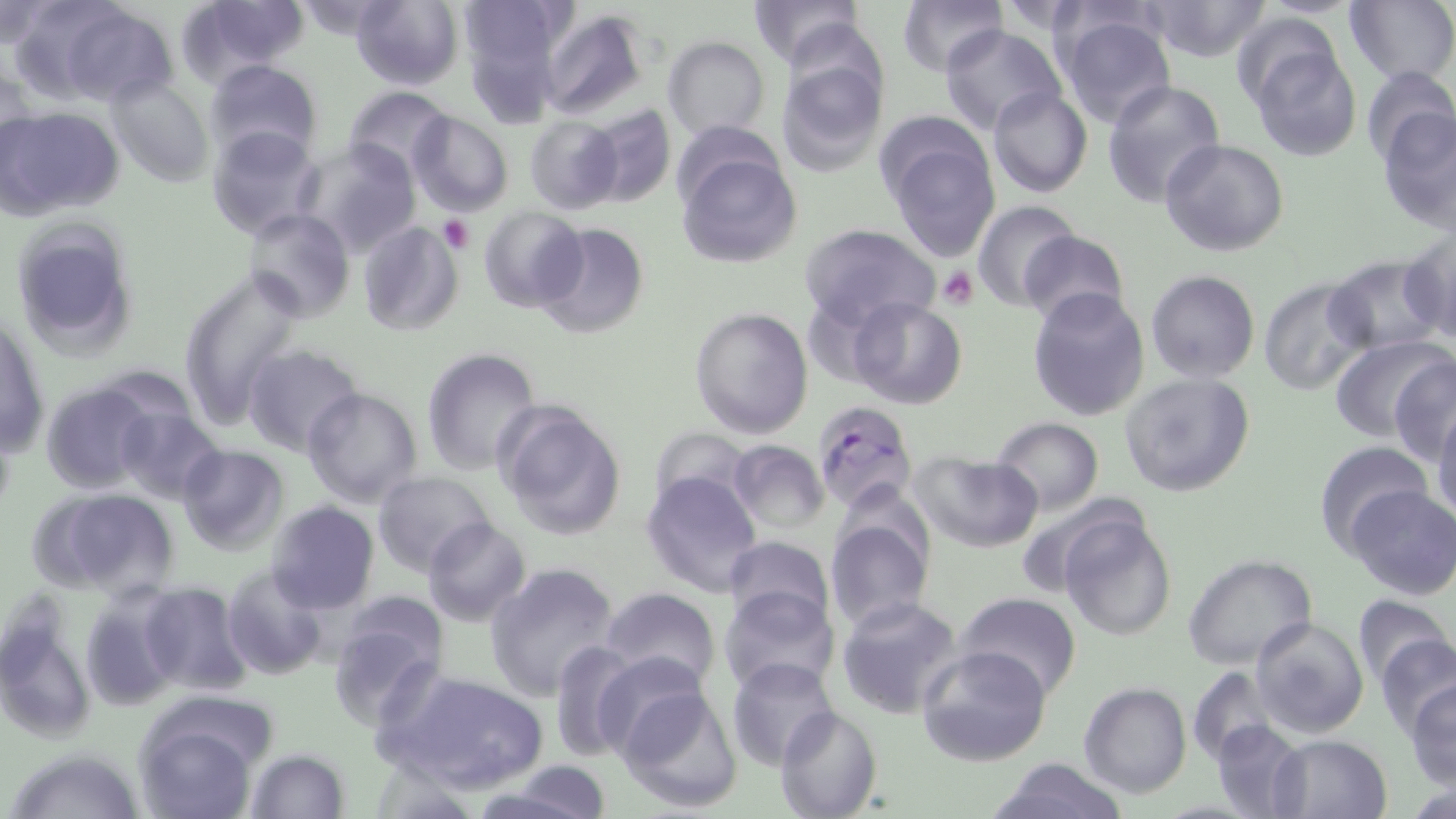
slide_level_diagnosis: Plasmodium falciparum
image_size: 1456×819 pixels
plasmodium_falciparum_infected_red_blood_cell_locations: 'approximate bounding boxes as [x1, y1, x2, y2] in pixels: [812, 401, 918, 514]'
platelet_locations: 'approximate bounding boxes as [x1, y1, x2, y2] in pixels: [439, 216, 474, 254], [938, 266, 979, 309]'
stain: May-Grünwald-Giemsa
magnification: 1000x
uninfected_red_blood_cell_locations: 'approximate bounding boxes as [x1, y1, x2, y2] in pixels: [174, 0, 307, 86], [353, 0, 463, 90], [747, 0, 862, 69], [896, 0, 1007, 77], [1144, 0, 1275, 62], [1, 2, 56, 49], [457, 2, 577, 66], [985, 2, 1103, 34], [1345, 2, 1456, 87], [55, 4, 176, 107], [539, 9, 651, 122], [1228, 11, 1344, 109], [1058, 12, 1178, 128], [938, 24, 1065, 132], [663, 36, 769, 141], [1244, 41, 1362, 162], [776, 58, 886, 178], [204, 59, 321, 164], [0, 63, 35, 173], [1359, 66, 1455, 166], [108, 76, 214, 188], [1101, 79, 1225, 208], [987, 85, 1093, 198], [344, 87, 451, 179], [580, 105, 677, 209], [1376, 105, 1456, 233], [1, 107, 123, 216], [408, 112, 513, 216], [524, 117, 623, 214], [512, 121, 611, 287], [207, 124, 321, 238], [882, 128, 1001, 261], [1160, 138, 1290, 257], [298, 140, 421, 259], [675, 144, 801, 270], [973, 200, 1081, 311], [479, 205, 587, 313], [243, 208, 353, 324], [8, 217, 143, 358], [357, 221, 464, 336], [534, 222, 649, 338], [800, 222, 940, 331], [1401, 228, 1456, 344], [1017, 229, 1129, 327], [1325, 257, 1444, 357], [176, 268, 309, 430], [1147, 271, 1259, 383], [1258, 277, 1378, 396], [1026, 289, 1151, 421], [848, 297, 968, 410], [689, 307, 813, 438], [0, 310, 49, 463], [1329, 336, 1453, 446], [243, 346, 360, 453], [422, 349, 542, 476], [1389, 355, 1456, 461], [1119, 373, 1257, 497], [40, 382, 160, 495], [301, 386, 423, 509], [495, 399, 627, 542], [1431, 401, 1456, 527], [113, 405, 225, 504], [992, 418, 1103, 514], [649, 428, 752, 512], [728, 440, 830, 535], [1314, 442, 1435, 556], [177, 443, 288, 554], [909, 451, 1044, 553], [640, 469, 763, 596], [373, 472, 494, 577], [1346, 485, 1456, 599], [30, 486, 181, 602], [1011, 492, 1145, 598], [265, 503, 379, 615], [1057, 513, 1177, 642], [825, 515, 933, 633], [423, 517, 530, 626], [722, 535, 834, 635], [1182, 554, 1317, 672], [484, 562, 619, 700], [224, 564, 329, 680], [133, 581, 252, 697], [602, 587, 722, 694], [717, 587, 839, 697], [957, 592, 1083, 701], [1350, 594, 1453, 689], [326, 596, 451, 731], [836, 596, 964, 718], [1250, 616, 1369, 738], [0, 617, 96, 744], [1374, 633, 1456, 738], [550, 639, 642, 761], [917, 645, 1051, 767], [591, 650, 708, 758], [726, 657, 840, 771], [1187, 666, 1277, 763], [386, 668, 549, 792], [1405, 679, 1456, 788], [1079, 683, 1191, 799], [615, 685, 743, 813], [774, 705, 883, 819], [137, 717, 261, 816], [1211, 717, 1306, 819], [1269, 733, 1391, 818], [7, 747, 146, 819], [245, 749, 350, 818], [987, 758, 1129, 819], [499, 763, 613, 819]'
modality: optical microscopy
field_of_view: single
preparation: thin blood smear